Assess this cell for malaria.
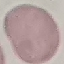
Uninfected.

Acquired by smartphone through the microscope eyepiece. Thin blood smear. Giemsa stain. Cell patch, automatically extracted from a larger field of view and resized to 64 × 64 pixels.